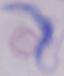
identification: trypanosome
magnification: 1000x
modality: micrograph